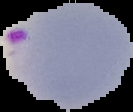 The area outside the segmented cell region is set to black. Image is 133×112 pixels. From a thin blood film. Malaria status: parasitized.